Mark where platelets are.
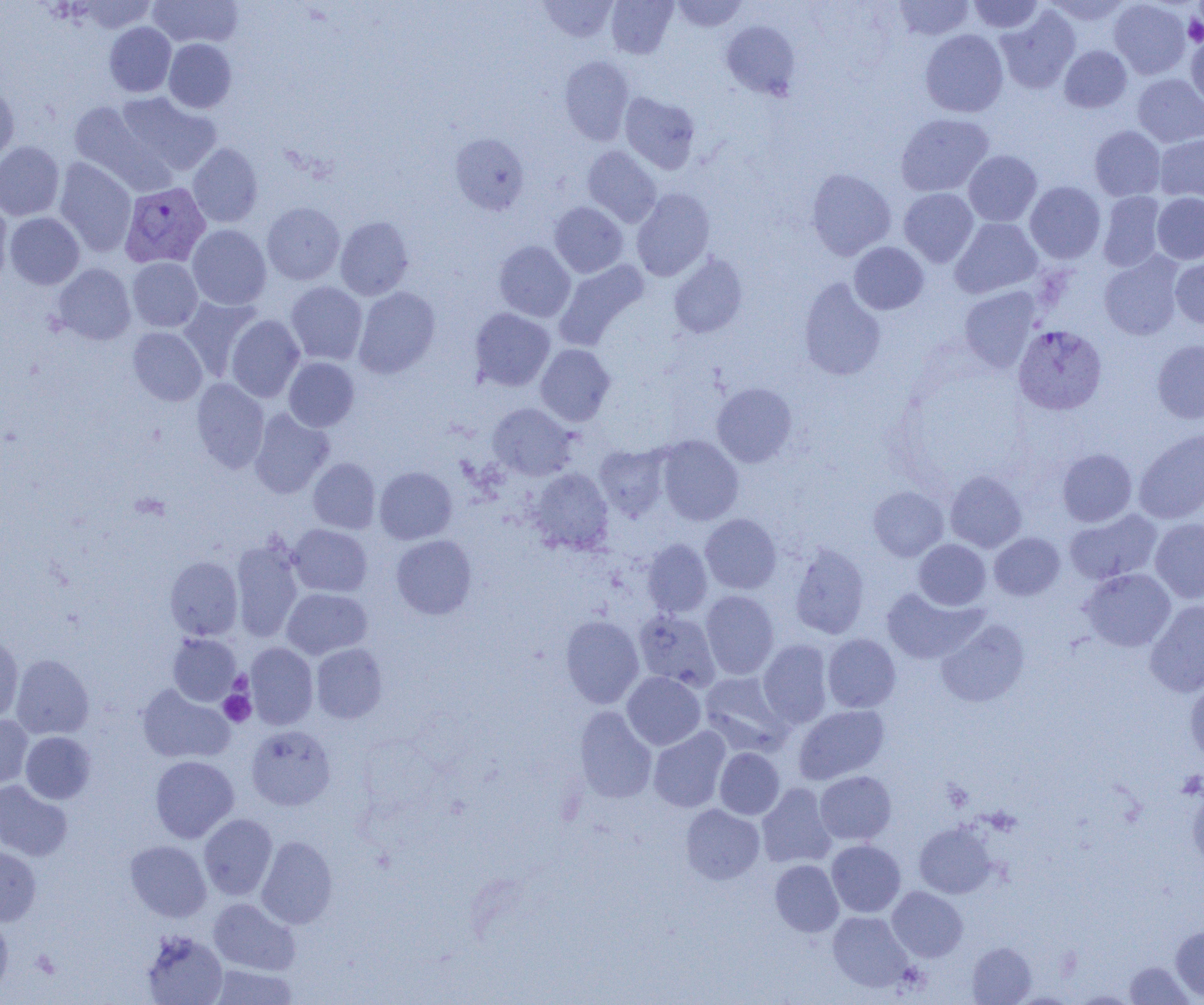
Approximate bounding boxes as (x1, y1, x2, y2) in pixels.
Platelets: (1184, 14, 1204, 46), (229, 671, 252, 695), (219, 690, 255, 726), (1177, 771, 1204, 799).

slide_level_diagnosis: Plasmodium vivax
field_of_view: one of a larger specimen
uninfected_red_blood_cell_locations: 'approximate bounding boxes as (x1, y1, x2, y2) in pixels: (76, 0, 157, 33), (148, 0, 243, 48), (538, 0, 617, 42), (606, 0, 677, 58), (671, 0, 748, 31), (893, 0, 975, 40), (969, 0, 1044, 33), (1044, 0, 1131, 26), (1110, 0, 1191, 78), (996, 6, 1080, 93), (721, 20, 800, 99), (104, 22, 176, 97), (920, 29, 1009, 117), (1186, 35, 1204, 109), (164, 38, 236, 113), (1059, 45, 1132, 113), (559, 56, 634, 145), (1133, 73, 1204, 147), (0, 86, 19, 166), (116, 92, 221, 175), (620, 92, 700, 173), (69, 101, 166, 191), (896, 113, 993, 197), (1089, 126, 1165, 201), (450, 133, 529, 214), (1154, 135, 1204, 202), (0, 141, 65, 220), (188, 143, 263, 227), (582, 146, 661, 227), (963, 150, 1042, 226), (54, 158, 137, 256), (806, 168, 896, 260), (1025, 181, 1105, 263), (632, 188, 714, 281), (899, 188, 979, 267), (1098, 192, 1165, 271), (1152, 193, 1204, 264), (0, 201, 12, 289), (262, 202, 344, 285), (549, 202, 628, 277), (4, 212, 85, 289), (335, 216, 414, 300), (951, 218, 1042, 298), (187, 224, 271, 310), (493, 241, 575, 322), (849, 242, 929, 314), (1099, 252, 1183, 340), (668, 253, 748, 339), (1170, 254, 1204, 330), (127, 257, 202, 332), (555, 259, 649, 349), (53, 263, 136, 345), (798, 277, 886, 381), (286, 281, 367, 365), (353, 286, 440, 378), (959, 286, 1040, 372), (178, 296, 262, 381), (469, 308, 555, 391), (226, 315, 305, 402), (128, 327, 207, 406), (1152, 339, 1204, 423), (536, 344, 615, 426), (283, 357, 359, 431), (192, 378, 269, 473), (712, 382, 796, 467), (488, 403, 577, 480), (249, 408, 334, 498), (1134, 429, 1204, 523), (656, 435, 744, 525), (594, 444, 670, 520), (1057, 448, 1137, 526), (308, 457, 380, 534), (374, 467, 457, 544), (529, 468, 613, 554), (945, 470, 1027, 552), (868, 486, 949, 561), (1065, 509, 1162, 585), (700, 513, 781, 594), (1150, 518, 1204, 603), (289, 524, 372, 597), (989, 532, 1065, 600), (391, 534, 477, 619), (642, 538, 712, 617), (230, 539, 303, 641), (913, 539, 991, 610), (789, 541, 869, 639), (165, 556, 242, 639), (1080, 568, 1176, 652), (880, 586, 986, 664), (282, 588, 372, 660), (701, 590, 779, 679), (1145, 600, 1204, 697), (634, 609, 720, 690), (561, 615, 644, 708), (936, 619, 1029, 707), (167, 633, 241, 706), (823, 634, 901, 712), (0, 636, 24, 723), (758, 639, 833, 728), (246, 642, 318, 729), (311, 643, 387, 723), (10, 654, 93, 739), (622, 672, 705, 750), (699, 672, 791, 755), (1185, 679, 1204, 764), (137, 684, 234, 764), (794, 705, 889, 784), (575, 706, 657, 803), (0, 714, 33, 788), (246, 725, 336, 811), (648, 726, 730, 812), (21, 732, 96, 804), (715, 748, 785, 819), (150, 755, 239, 843), (815, 770, 896, 845), (0, 780, 72, 861), (757, 783, 836, 868), (1188, 787, 1204, 871), (681, 804, 765, 884), (199, 814, 277, 900), (914, 822, 996, 898), (257, 836, 337, 928), (125, 840, 212, 922), (826, 840, 906, 917), (0, 845, 41, 926), (770, 860, 844, 936), (887, 886, 967, 961), (208, 897, 300, 975), (828, 911, 913, 991), (0, 913, 13, 998), (1170, 925, 1204, 1002), (140, 930, 227, 1005), (967, 941, 1036, 1004), (1125, 961, 1193, 1004), (207, 964, 298, 1004), (1070, 990, 1140, 1004)'
preparation: thin blood smear
modality: optical microscopy
magnification: 1000x
plasmodium_vivax_infected_red_blood_cell_locations: 'approximate bounding boxes as (x1, y1, x2, y2) in pixels: (120, 181, 211, 268), (1013, 324, 1106, 415)'
image_size: 1204×1005 pixels